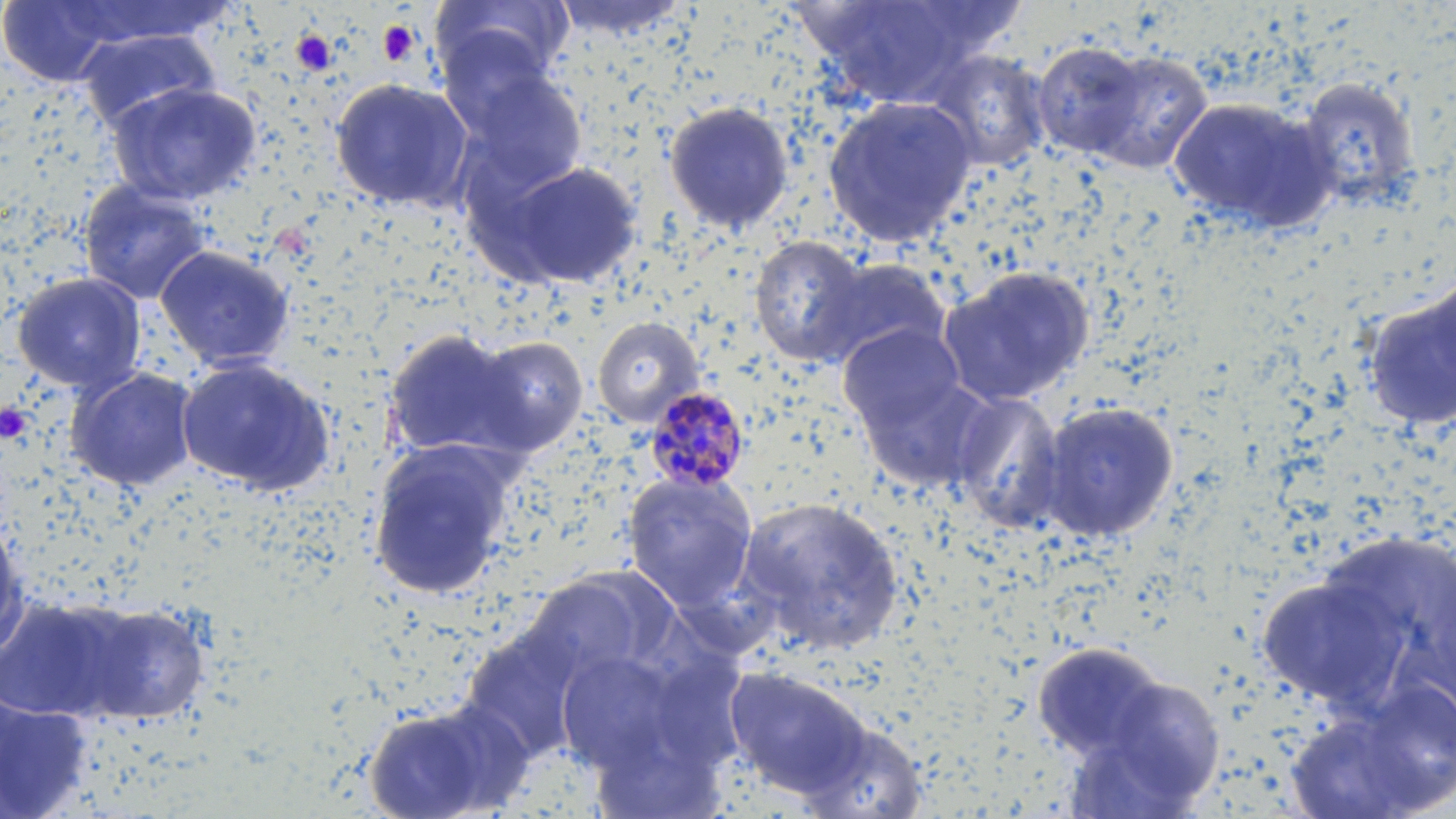

Approximate bounding boxes as (x1,y1)-(x2,y2) corner pairs in pixels. Platelet locations: (377,19)-(421,65), (291,29)-(338,78), (0,402)-(33,443). Uninfected red blood cell locations: (55,0)-(234,47), (434,0)-(572,94), (551,0)-(691,41), (803,0)-(997,108), (0,1)-(123,86), (75,27)-(220,132), (1032,41)-(1149,160), (1080,49)-(1213,175), (922,50)-(1052,173), (448,61)-(588,201), (1295,76)-(1421,214), (330,77)-(475,213), (106,81)-(263,206), (822,96)-(978,248), (1168,96)-(1335,233), (663,101)-(795,235), (486,159)-(644,290), (78,180)-(213,306), (749,235)-(870,367), (154,243)-(296,372), (810,258)-(952,371), (937,266)-(1094,407), (10,271)-(147,395), (1362,279)-(1456,433), (592,316)-(705,427), (838,323)-(968,438), (381,327)-(532,465), (465,334)-(589,456), (175,356)-(336,497), (65,367)-(200,492), (857,368)-(998,493), (950,392)-(1067,531), (1036,400)-(1180,545), (367,439)-(520,600), (622,472)-(759,614), (734,496)-(907,657), (0,512)-(29,659), (1257,556)-(1427,717), (522,573)-(663,687), (0,594)-(150,724), (460,624)-(589,766), (1031,641)-(1169,763), (553,647)-(694,782), (724,666)-(874,800), (1092,670)-(1226,808), (0,694)-(92,817), (360,699)-(521,819), (794,714)-(931,819). Plasmodium malariae-infected red blood cell locations: (642,385)-(750,493). Slide-level diagnosis: Plasmodium malariae. Thin blood film. Single field of view. Image is 1456×819 pixels. 1000x magnification. Light microscopy. May-Grünwald-Giemsa-stained preparation.